Comment on the morphology of the erythrocytes.
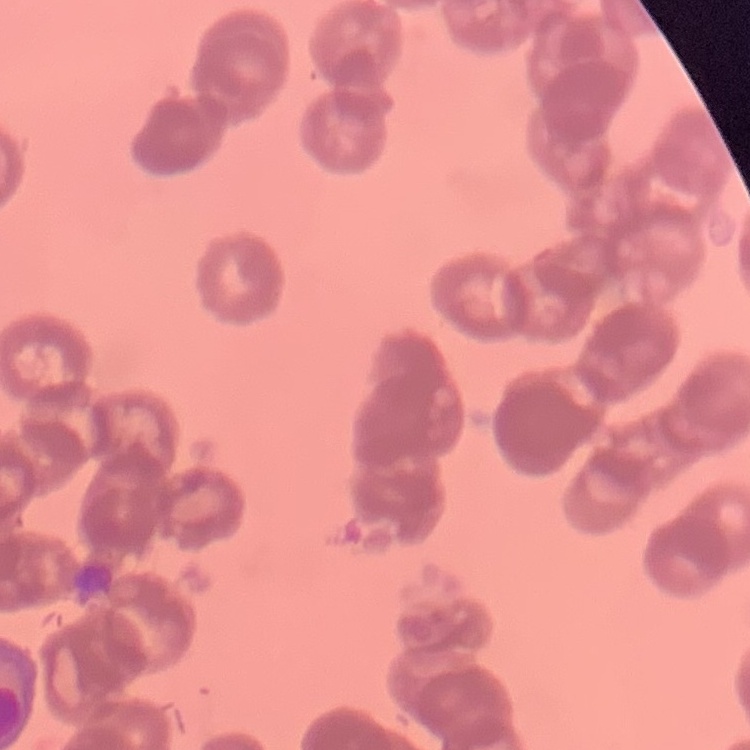

Rouleaux formation.

preparation = thin blood smear
image type = one tile cut from a larger photomicrograph
stain = Field's or Giemsa